Classify this cell by malaria status.
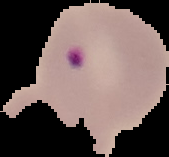

Parasitized.

image size = 169×157 pixels
preparation = thin blood film
image type = cell region segmented out of the field of view; surrounding area masked to black